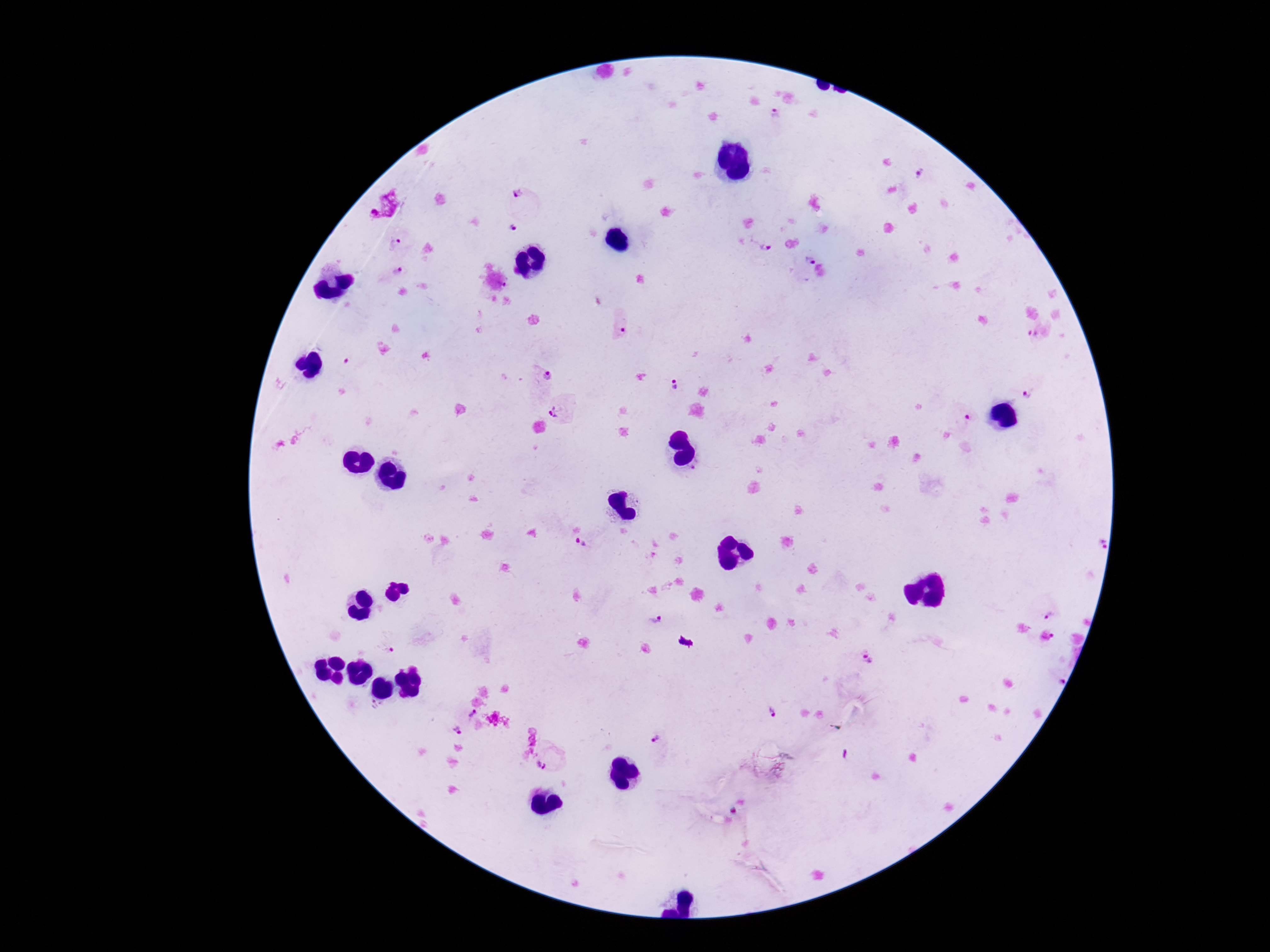
Approximate centers as (x, y) in pixels. Plasmodium parasite locations: (776, 114), (930, 172), (523, 201), (510, 233), (397, 243), (763, 248), (806, 261), (401, 274), (506, 285), (620, 328), (1032, 337), (547, 375), (675, 385), (1033, 387), (560, 410), (962, 420), (583, 542), (1050, 608), (659, 625), (1057, 635), (384, 645), (868, 661), (1060, 677), (374, 706), (773, 712), (466, 715), (455, 734), (658, 744), (550, 757). 100x magnification. Image is 1270×952 pixels. Patient malaria status: positive. Giemsa stain. One field from this slide. Photographed through the microscope eyepiece with a smartphone camera. Thick blood film.